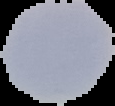
Summary:
  - Image type: cell region segmented out of the field of view; surrounding area masked to black
  - Image size: 115×106 pixels
  - Result: no Plasmodium parasites detected
  - Preparation: thin blood smear